Assess the morphology of the erythrocytes.
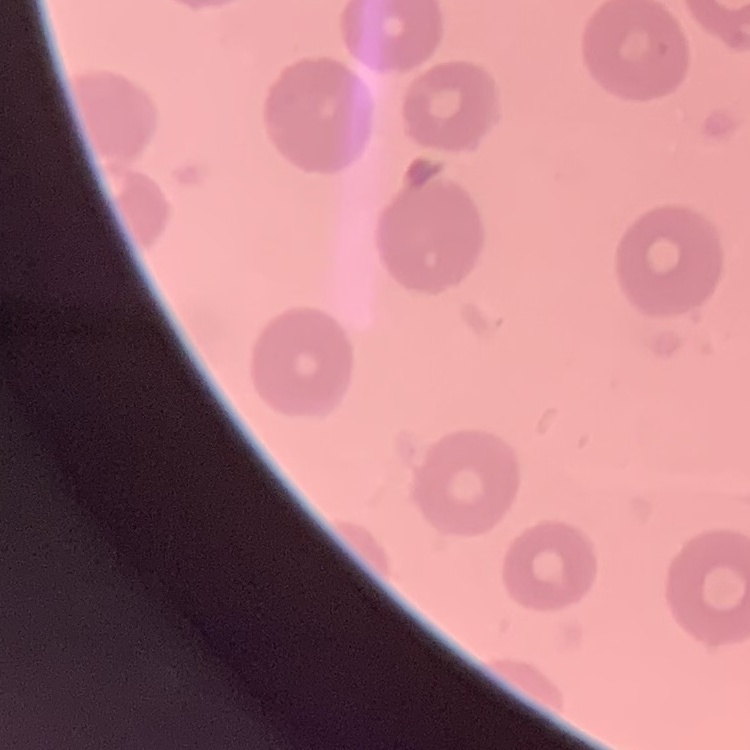

They show no rouleaux formation.

Stained with either Field's or Giemsa. Thin blood smear. One tile cut from a larger photomicrograph.